Classify this cell by malaria status.
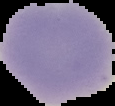

Uninfected.

Image is 115×106 pixels. From a thin blood smear. The area outside the segmented cell region is set to black.